Point out each Plasmodium parasite.
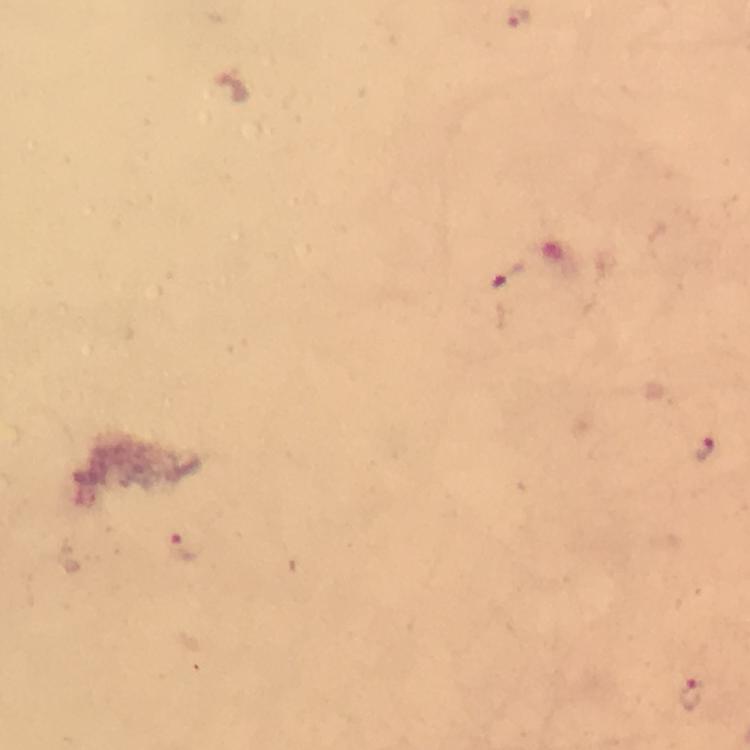
Approximate centers as (x, y) in pixels.
Plasmodium parasites: (516, 18), (508, 276), (705, 448), (180, 547), (694, 693).

Thick blood film. Giemsa stain. From a malaria diagnostic workup. Image is 750×750 pixels. Smartphone photograph taken through a microscope. At 100x magnification. Immersion oil was used. Cropped region of a single field of view.